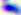 Captured at 400x magnification. Photomicrograph. Toxoplasma gondii is seen.